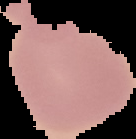

Result: no malaria parasites seen. From a thin blood film. Cell region segmented out of the field of view; the surrounding area is masked to black. Image is 136×139 pixels.